Locate every Plasmodium falciparum parasite and give its life-cycle stage, and locate every leukocyte and any debris.
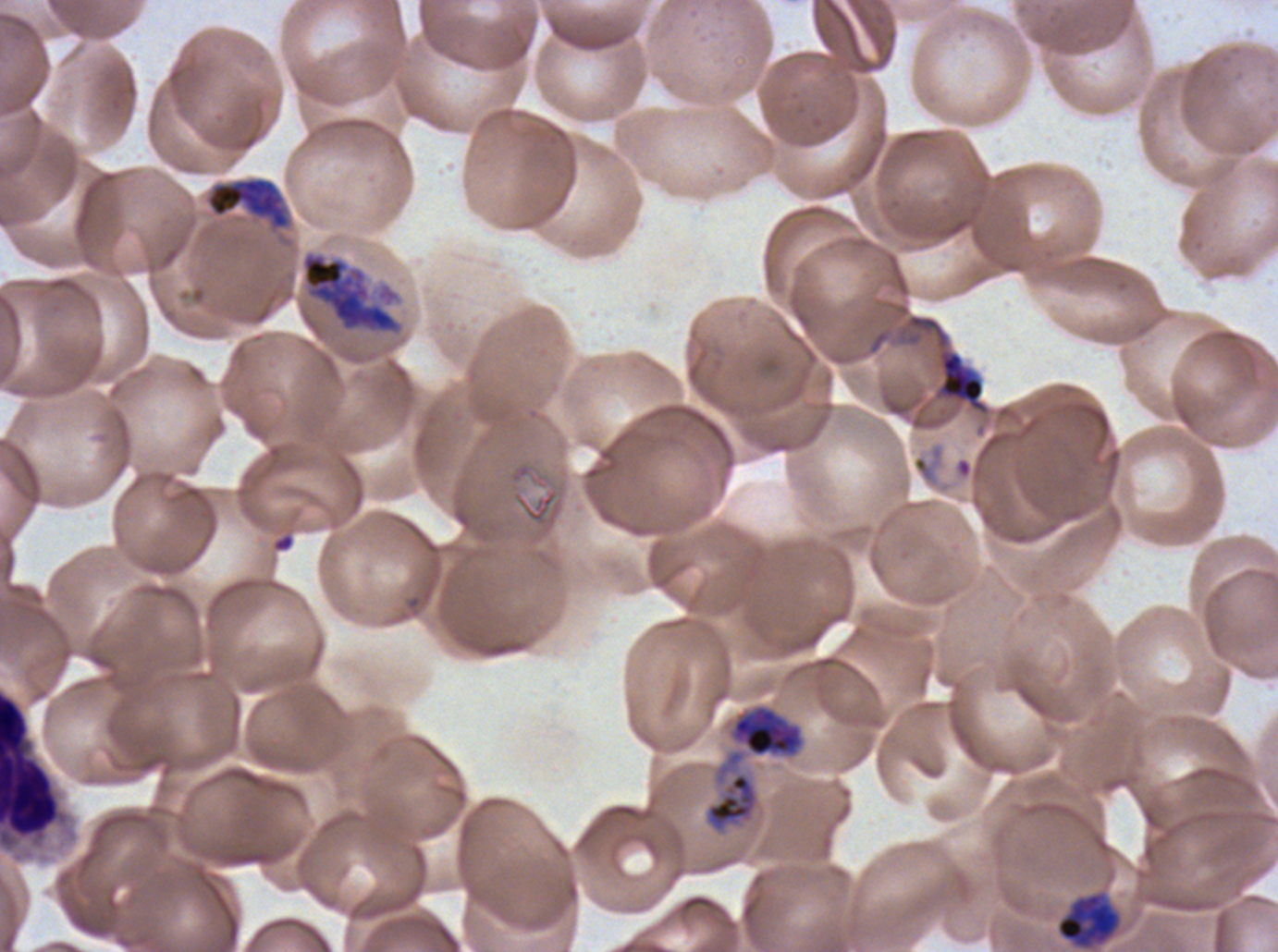

Approximate bounding boxes as {x1, y1, x2, y2} in pixels.
Late trophozoites: {206, 177, 289, 228}.
Early schizonts: {1056, 893, 1120, 947}.
Late schizonts: {300, 250, 404, 336}, {704, 705, 803, 835}.
Leukocytes: {0, 689, 62, 848}.
Debris: {940, 353, 984, 403}.
No rings, late-ring/early-trophozoite forms, mid trophozoites, segmenters, or gametocytes observed.

Image is 1278×952 pixels. Life-cycle stages observed: late trophozoite, early schizont, late schizont. Plasmodium falciparum cultured ex vivo for 24 to 48 hours, from a patient in The Gambia. Giemsa stain. Thin blood film. A sub-image separated from a larger composite.